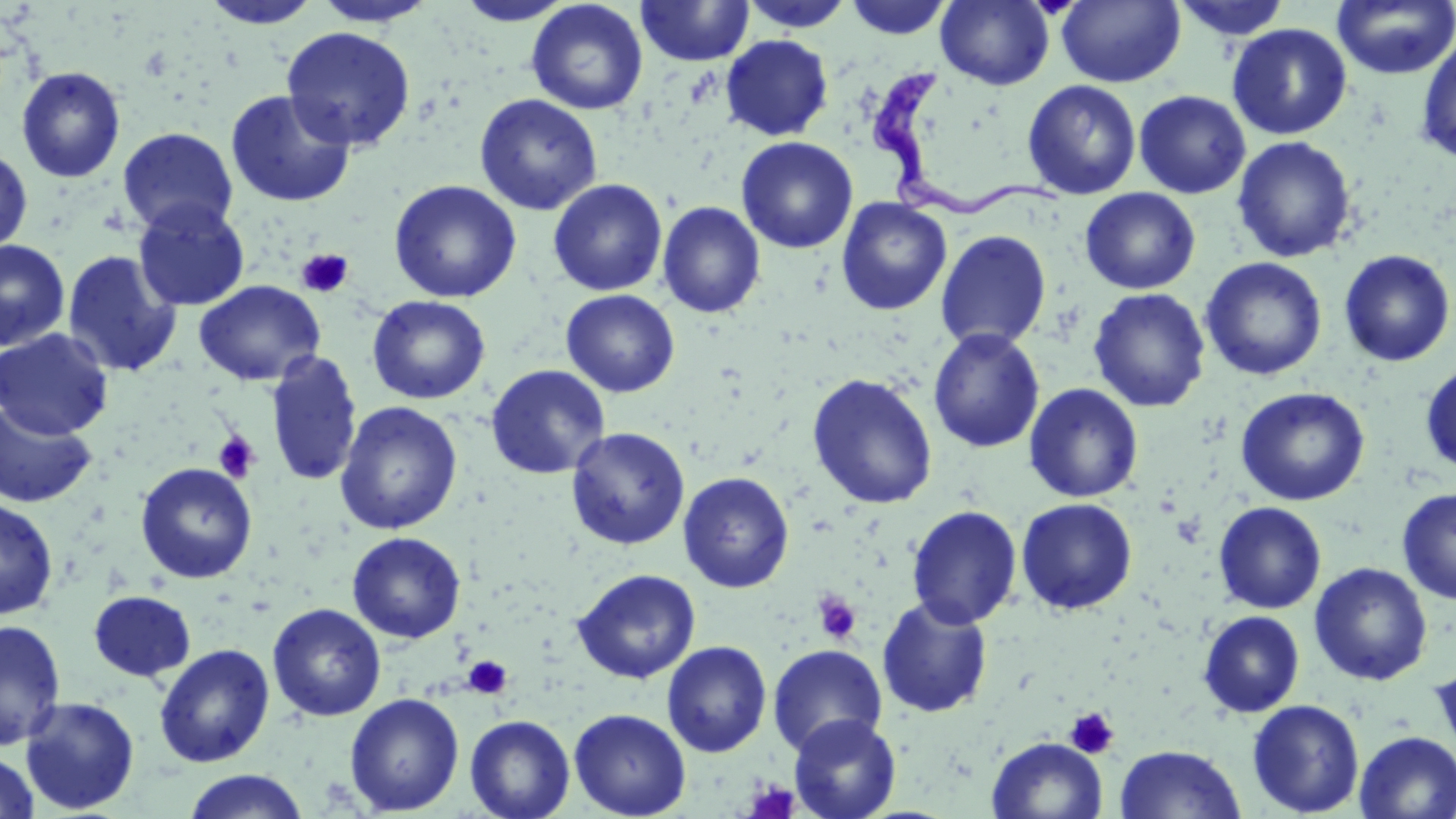

slide-level diagnosis = Trypanosoma brucei
field of view = single
platelet locations = approximate bounding boxes as named x1/y1/x2/y2 corners in pixels: (x1=295, y1=249, x2=354, y2=298), (x1=213, y1=431, x2=260, y2=482), (x1=812, y1=592, x2=862, y2=645), (x1=463, y1=655, x2=513, y2=699), (x1=1064, y1=707, x2=1120, y2=759), (x1=744, y1=778, x2=800, y2=819)
image size = 1456×819 pixels
preparation = thin blood film
Trypanosoma brucei locations = approximate bounding boxes as named x1/y1/x2/y2 corners in pixels: (x1=866, y1=67, x2=1067, y2=219)
uninfected red blood cell locations = approximate bounding boxes as named x1/y1/x2/y2 corners in pixels: (x1=526, y1=0, x2=648, y2=115), (x1=740, y1=0, x2=856, y2=32), (x1=845, y1=0, x2=952, y2=40), (x1=936, y1=0, x2=1054, y2=90), (x1=1056, y1=0, x2=1185, y2=88), (x1=1172, y1=0, x2=1293, y2=40), (x1=1331, y1=0, x2=1456, y2=79), (x1=199, y1=1, x2=322, y2=29), (x1=312, y1=1, x2=438, y2=28), (x1=454, y1=1, x2=575, y2=26), (x1=636, y1=1, x2=754, y2=67), (x1=1227, y1=23, x2=1352, y2=140), (x1=280, y1=26, x2=416, y2=151), (x1=721, y1=34, x2=833, y2=141), (x1=1415, y1=34, x2=1456, y2=164), (x1=16, y1=66, x2=126, y2=183), (x1=1022, y1=80, x2=1141, y2=200), (x1=225, y1=89, x2=356, y2=208), (x1=1134, y1=90, x2=1251, y2=198), (x1=474, y1=94, x2=602, y2=216), (x1=117, y1=127, x2=239, y2=236), (x1=736, y1=136, x2=858, y2=254), (x1=1231, y1=136, x2=1357, y2=263), (x1=0, y1=148, x2=33, y2=256), (x1=548, y1=178, x2=667, y2=296), (x1=388, y1=180, x2=522, y2=303), (x1=1080, y1=188, x2=1200, y2=294), (x1=836, y1=197, x2=952, y2=315), (x1=132, y1=200, x2=251, y2=311), (x1=657, y1=201, x2=766, y2=318), (x1=935, y1=230, x2=1052, y2=351), (x1=0, y1=239, x2=70, y2=351), (x1=62, y1=249, x2=182, y2=378), (x1=1338, y1=249, x2=1454, y2=367), (x1=1200, y1=257, x2=1327, y2=381), (x1=194, y1=280, x2=325, y2=386), (x1=1088, y1=287, x2=1211, y2=413), (x1=561, y1=289, x2=680, y2=397), (x1=367, y1=295, x2=490, y2=404), (x1=0, y1=328, x2=114, y2=440), (x1=928, y1=328, x2=1045, y2=453), (x1=265, y1=351, x2=362, y2=488), (x1=1420, y1=363, x2=1456, y2=474), (x1=486, y1=364, x2=610, y2=480), (x1=806, y1=373, x2=939, y2=510), (x1=1024, y1=383, x2=1143, y2=503), (x1=1235, y1=387, x2=1370, y2=506), (x1=0, y1=402, x2=97, y2=509), (x1=335, y1=402, x2=462, y2=535), (x1=566, y1=426, x2=690, y2=551), (x1=135, y1=462, x2=257, y2=583), (x1=678, y1=471, x2=794, y2=593), (x1=1396, y1=487, x2=1456, y2=604), (x1=0, y1=498, x2=59, y2=620), (x1=1016, y1=498, x2=1138, y2=615), (x1=1213, y1=501, x2=1326, y2=614), (x1=906, y1=505, x2=1023, y2=629), (x1=347, y1=532, x2=465, y2=643), (x1=1309, y1=562, x2=1432, y2=686), (x1=572, y1=568, x2=701, y2=684), (x1=88, y1=590, x2=196, y2=682), (x1=876, y1=597, x2=993, y2=718), (x1=267, y1=602, x2=387, y2=722), (x1=1198, y1=610, x2=1305, y2=717), (x1=0, y1=620, x2=66, y2=750), (x1=661, y1=641, x2=772, y2=758), (x1=154, y1=644, x2=275, y2=768), (x1=767, y1=644, x2=887, y2=757), (x1=1429, y1=661, x2=1456, y2=762), (x1=344, y1=692, x2=464, y2=815), (x1=19, y1=696, x2=140, y2=815), (x1=1246, y1=699, x2=1365, y2=817), (x1=568, y1=708, x2=691, y2=819), (x1=464, y1=714, x2=575, y2=819), (x1=788, y1=714, x2=901, y2=819), (x1=1354, y1=731, x2=1456, y2=818), (x1=987, y1=736, x2=1107, y2=818), (x1=1114, y1=744, x2=1247, y2=819), (x1=0, y1=751, x2=40, y2=819), (x1=181, y1=770, x2=310, y2=819)
modality = optical microscopy
magnification = 1000x
stain = May-Grünwald-Giemsa